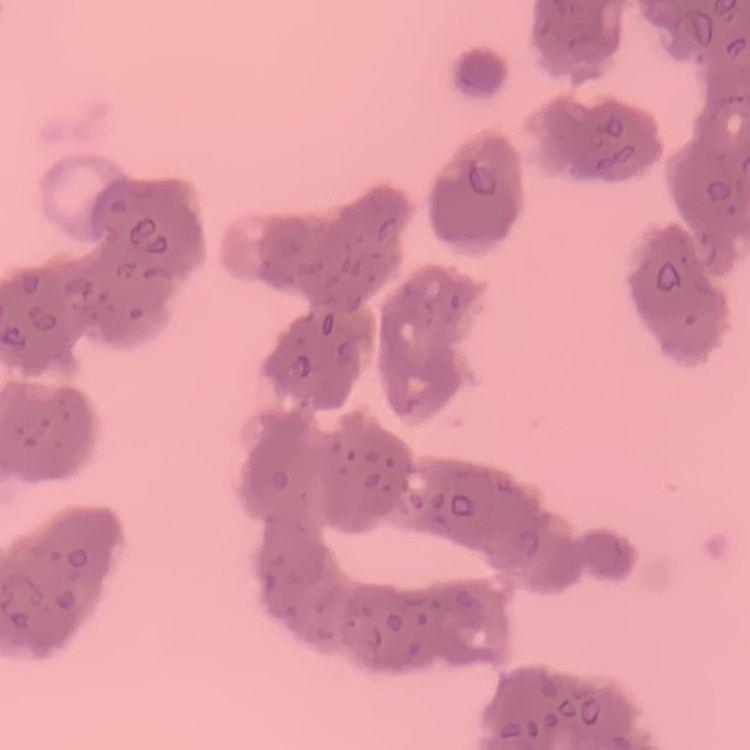

erythrocyte morphology = rouleaux formation
preparation = thin peripheral smear
image type = square crop of a larger photomicrograph
stain = Field's or Giemsa